State which parasite is depicted.
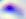

Toxoplasma gondii.

modality = micrograph
magnification = 400x